Locate every blood parasite and identify its species.
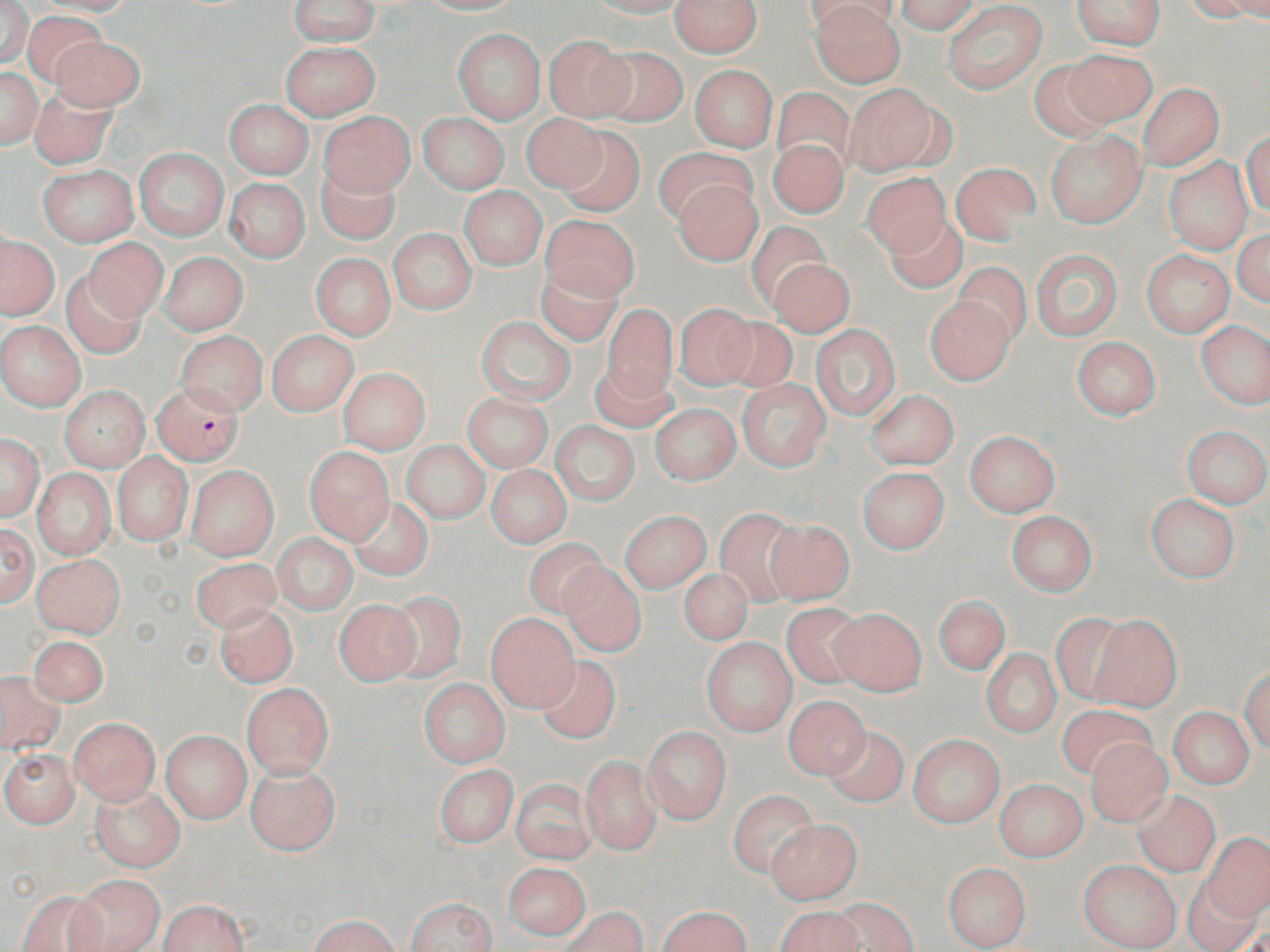

Approximate bounding boxes as [x1, y1, x2, y2] in pixels.
Plasmodium falciparum-infected red blood cells: [153, 380, 244, 466].
No Plasmodium ovale, Plasmodium malariae, Plasmodium vivax, Babesia divergens, or Trypanosoma brucei observed.

{
  "slide_level_diagnosis": "Plasmodium falciparum",
  "preparation": "thin blood smear",
  "uninfected_red_blood_cell_locations": "approximate bounding boxes as [x1, y1, x2, y2] in pixels: [30, 0, 142, 16], [290, 0, 380, 45], [417, 0, 523, 15], [587, 0, 690, 16], [669, 0, 763, 57], [802, 0, 901, 33], [894, 0, 979, 34], [1071, 0, 1166, 49], [1185, 0, 1270, 20], [941, 1, 1048, 93], [1, 2, 34, 66], [810, 3, 907, 87], [24, 12, 107, 86], [453, 28, 544, 124], [543, 35, 635, 122], [50, 36, 146, 112], [281, 41, 381, 119], [596, 46, 687, 126], [1059, 48, 1157, 130], [1027, 59, 1118, 141], [689, 64, 777, 152], [0, 67, 42, 148], [844, 83, 943, 174], [1138, 83, 1224, 170], [28, 86, 116, 168], [771, 88, 854, 173], [224, 99, 313, 178], [320, 111, 414, 197], [419, 113, 509, 193], [520, 113, 608, 194], [557, 126, 644, 217], [1243, 128, 1270, 219], [1045, 130, 1148, 227], [768, 137, 849, 218], [654, 148, 752, 225], [135, 149, 228, 239], [1164, 157, 1253, 254], [315, 163, 401, 245], [951, 163, 1040, 243], [38, 166, 138, 246], [861, 171, 951, 257], [673, 177, 763, 265], [225, 178, 310, 262], [459, 186, 547, 269], [542, 214, 639, 301], [883, 214, 967, 292], [746, 220, 834, 307], [1233, 226, 1270, 308], [388, 229, 476, 314], [0, 234, 60, 320], [85, 238, 168, 321], [1030, 246, 1124, 343], [1141, 248, 1235, 338], [157, 252, 249, 335], [310, 253, 395, 340], [769, 258, 855, 336], [953, 263, 1031, 346], [537, 267, 622, 346], [61, 272, 146, 358], [924, 295, 1015, 386], [674, 303, 758, 391], [602, 305, 678, 398], [719, 315, 800, 394], [477, 317, 576, 404], [0, 321, 86, 411], [1197, 321, 1270, 409], [810, 324, 902, 421], [267, 330, 359, 415], [174, 331, 269, 417], [1071, 337, 1161, 419], [591, 360, 677, 432], [338, 367, 431, 453], [737, 378, 831, 471], [59, 386, 150, 472], [865, 390, 959, 469], [463, 394, 553, 472], [650, 404, 741, 484], [550, 422, 640, 505], [1181, 425, 1269, 509], [965, 431, 1061, 516], [0, 433, 44, 521], [402, 440, 491, 524], [304, 448, 394, 543], [112, 451, 194, 546], [186, 465, 279, 560], [486, 465, 572, 547], [32, 467, 115, 559], [857, 467, 950, 552], [1145, 494, 1240, 582], [348, 496, 434, 581], [714, 509, 804, 606], [620, 511, 712, 593], [1005, 511, 1097, 596], [763, 518, 856, 605], [0, 523, 38, 607], [272, 535, 358, 613], [523, 538, 608, 617], [31, 553, 125, 640], [190, 557, 282, 632], [559, 562, 647, 656], [677, 568, 754, 645], [381, 589, 468, 684], [933, 595, 1011, 674], [334, 599, 421, 685], [781, 602, 868, 688], [215, 604, 298, 687], [829, 608, 927, 696], [1049, 613, 1131, 707], [486, 614, 579, 711], [1089, 616, 1183, 712], [29, 634, 109, 706], [702, 638, 797, 735], [981, 649, 1060, 736], [535, 654, 621, 743], [1240, 665, 1270, 755], [0, 670, 65, 758], [417, 677, 511, 767], [241, 683, 335, 781], [784, 695, 870, 777], [1056, 704, 1156, 782], [1168, 707, 1254, 789], [69, 718, 160, 804], [822, 725, 910, 808], [641, 727, 730, 823], [161, 730, 252, 823], [908, 735, 1005, 827], [1086, 737, 1173, 827], [0, 749, 80, 828], [579, 755, 662, 855], [244, 762, 342, 855], [434, 765, 518, 848], [993, 778, 1088, 862], [511, 779, 596, 864], [90, 785, 185, 872], [728, 789, 819, 880], [1132, 791, 1221, 878], [765, 819, 862, 903], [1201, 834, 1270, 920], [1078, 860, 1182, 951], [502, 863, 591, 939], [942, 863, 1031, 950], [67, 873, 166, 952], [1183, 877, 1262, 952], [15, 888, 109, 952], [405, 896, 498, 951], [831, 897, 918, 951], [157, 899, 249, 952], [776, 904, 864, 952], [656, 905, 751, 952], [557, 907, 648, 952], [310, 915, 400, 952]",
  "stain": "May-Grünwald-Giemsa",
  "magnification": "1000x",
  "field_of_view": "single",
  "modality": "light microscopy",
  "image_size": "1270×952 pixels"
}